Point out each Plasmodium parasite.
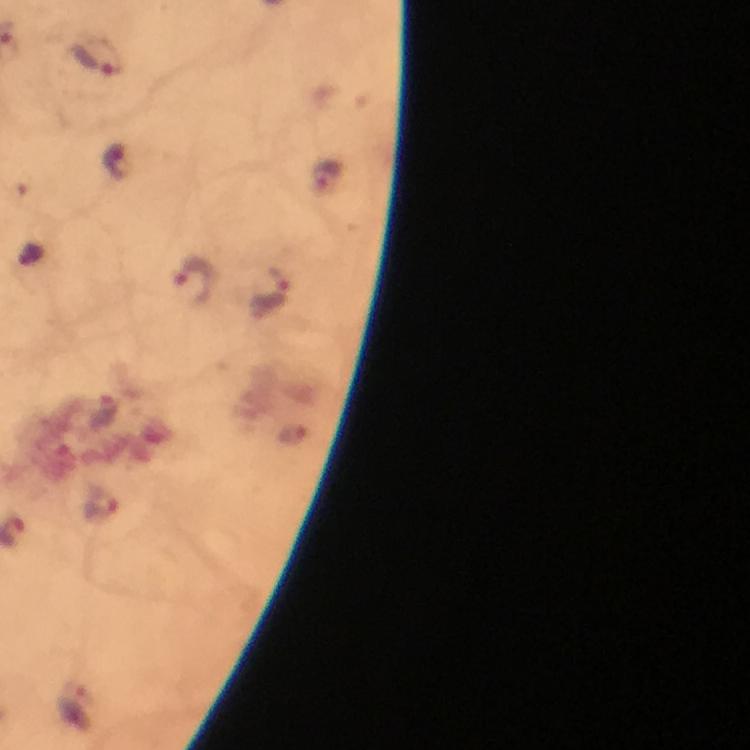
Approximate object centers, in pixels from the top-left corner.
Plasmodium parasites: (x=96, y=56), (x=195, y=281), (x=270, y=289), (x=100, y=505).

Summary:
  - Cropped from: a single field of view
  - Capture: smartphone camera through the microscope
  - Magnification: 100x
  - Immersion oil: used
  - Stain: Giemsa
  - Image size: 750×750 pixels
  - Preparation: thick blood smear
  - Context: from a malaria diagnostic workup